Identify the blood parasite species.
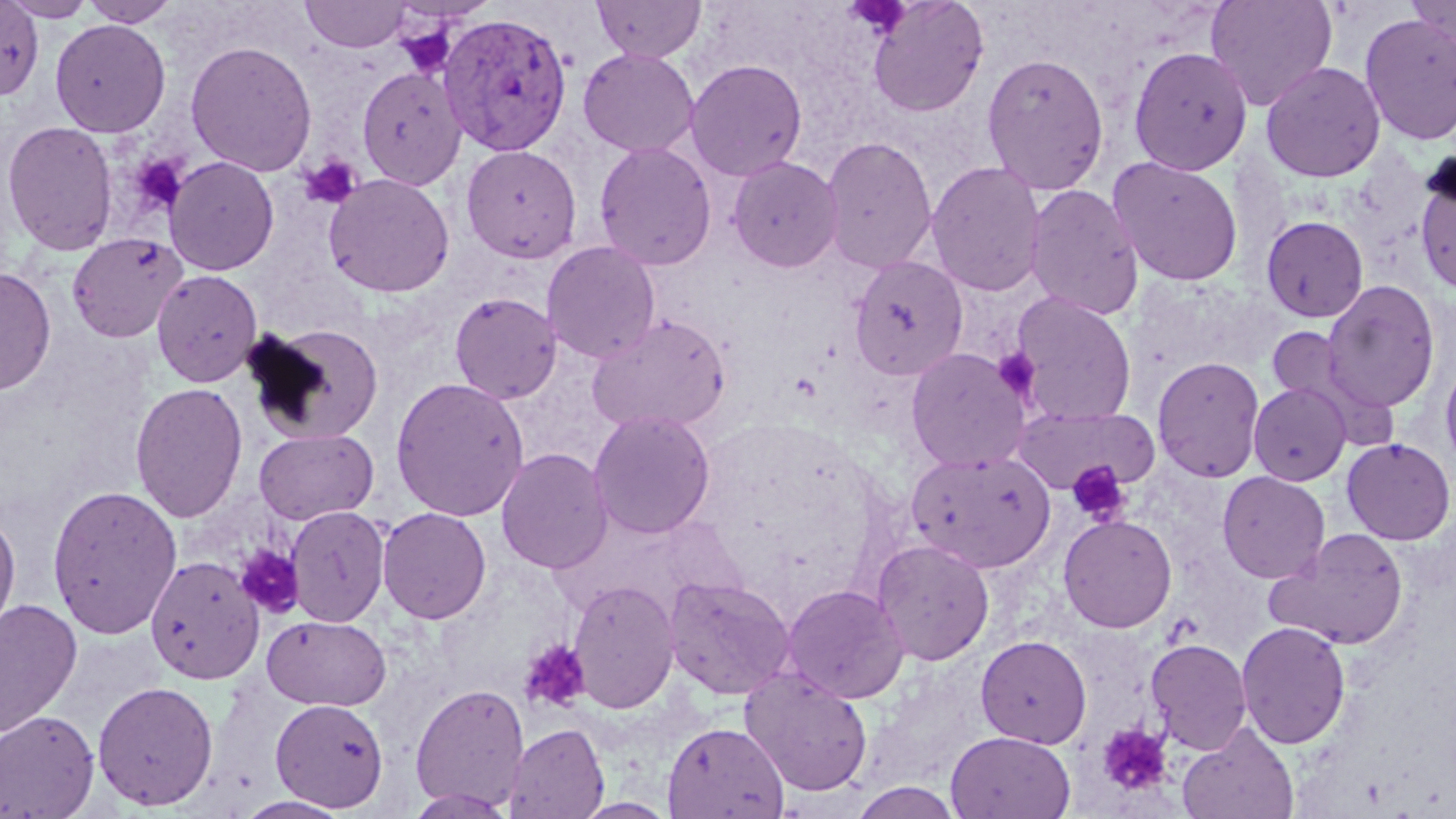
Plasmodium vivax.

Summary:
  - Coordinate format: approximate bounding boxes as (x1,y1)-(x2,y2) corner pairs in pixels
  - Plasmodium vivax-infected red blood cell locations: (439,11)-(573,157)
  - Uninfected red blood cell locations: (4,0)-(98,21), (79,0)-(180,27), (301,0)-(411,52), (591,0)-(706,61), (867,0)-(989,117), (1205,0)-(1337,111), (1406,0)-(1455,47), (0,1)-(44,101), (1359,13)-(1456,146), (49,19)-(171,137), (185,41)-(318,176), (1127,45)-(1253,176), (578,48)-(700,157), (981,51)-(1110,195), (685,59)-(807,180), (1260,61)-(1386,182), (356,66)-(466,190), (1,120)-(119,255), (821,135)-(937,274), (594,141)-(717,270), (461,145)-(582,263), (163,155)-(280,276), (727,155)-(842,273), (1107,155)-(1244,287), (926,161)-(1047,296), (1414,167)-(1456,296), (323,173)-(455,298), (1025,184)-(1144,320), (1260,215)-(1369,322), (66,232)-(188,343), (542,241)-(661,363), (849,255)-(969,381), (0,267)-(57,396), (151,269)-(263,387), (1321,280)-(1441,413), (449,292)-(562,404), (1010,292)-(1138,425), (586,313)-(732,434), (245,323)-(384,444), (1265,326)-(1351,407), (905,348)-(1031,472), (1152,356)-(1265,482), (1440,360)-(1456,472), (390,376)-(529,521), (130,382)-(248,523), (1248,382)-(1351,485), (1012,404)-(1159,494), (588,408)-(715,540), (253,428)-(379,525), (1341,437)-(1455,545), (496,447)-(613,575), (907,448)-(1056,573), (1216,471)-(1330,584), (46,484)-(182,639), (285,505)-(390,627), (0,507)-(21,644), (377,507)-(492,624), (1058,514)-(1177,632), (1267,527)-(1410,650), (871,539)-(994,665), (144,554)-(264,684), (663,576)-(796,700), (568,578)-(680,714), (782,584)-(909,704), (0,597)-(83,740), (263,614)-(391,711), (1236,621)-(1351,749), (976,635)-(1091,748), (1146,638)-(1252,754), (740,667)-(874,797), (92,679)-(219,811), (409,682)-(529,811), (270,697)-(389,811), (0,710)-(99,818), (662,721)-(789,819), (1177,722)-(1300,819), (503,723)-(609,819), (946,730)-(1075,818), (849,781)-(964,818), (403,789)-(518,818), (232,795)-(354,818), (574,797)-(677,818)
  - Platelet locations: (395,23)-(457,79), (131,155)-(188,215), (299,155)-(362,210), (993,347)-(1041,400), (1066,461)-(1130,524), (235,544)-(305,618), (519,638)-(592,713), (1097,723)-(1173,796)
  - Field of view: single
  - Stain: May-Grünwald-Giemsa
  - Preparation: thin blood film
  - Image size: 1456×819 pixels
  - Modality: optical microscopy
  - Magnification: 1000x